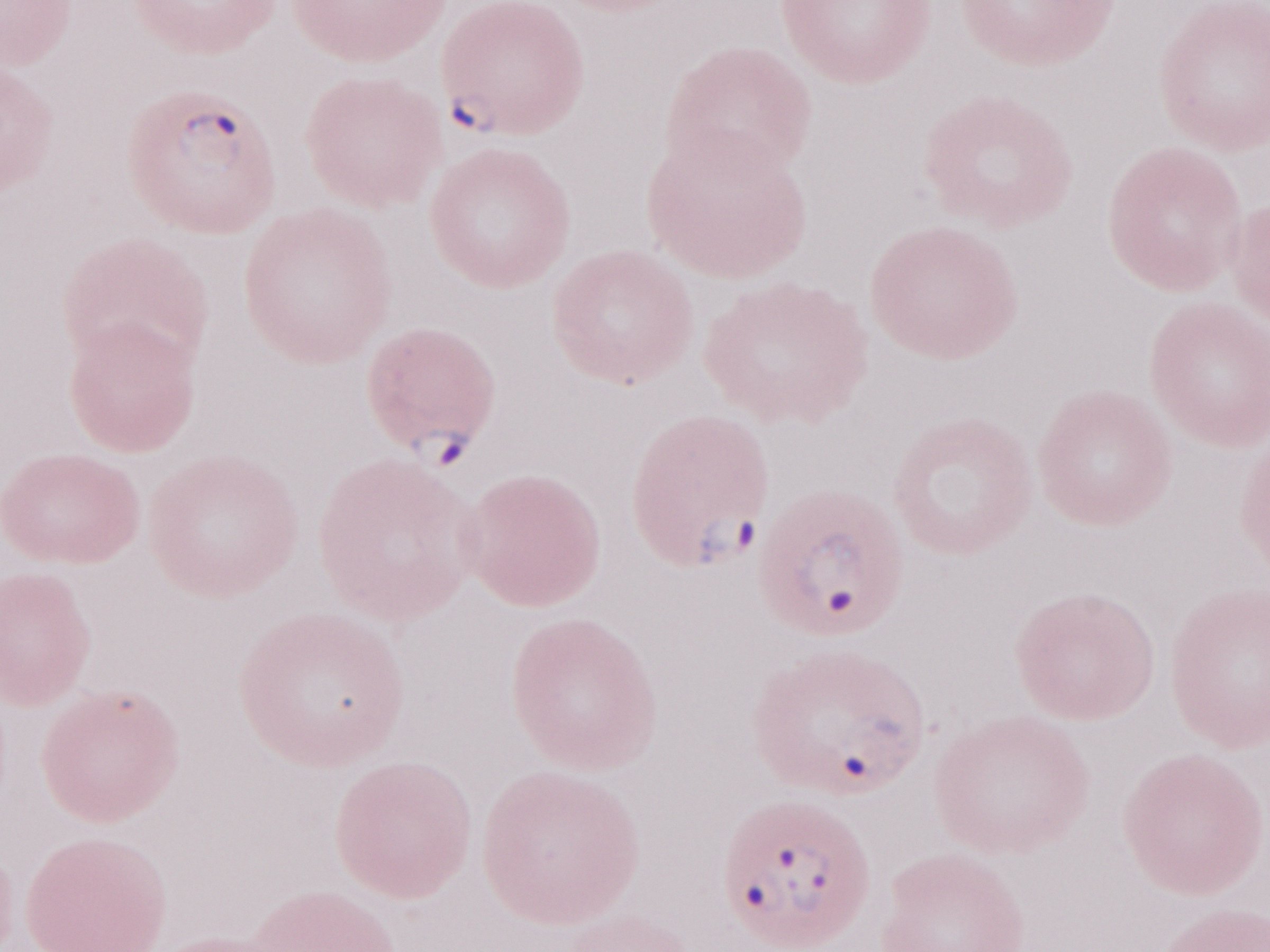
Patient diagnosis: malaria infection. Image is 1270×952 pixels. Magnification: 1,000x. Single field of view. May-Grünwald-Giemsa-stained preparation. Olympus BX43 microscope, Olympus DP73 camera. Thin peripheral-blood smear.